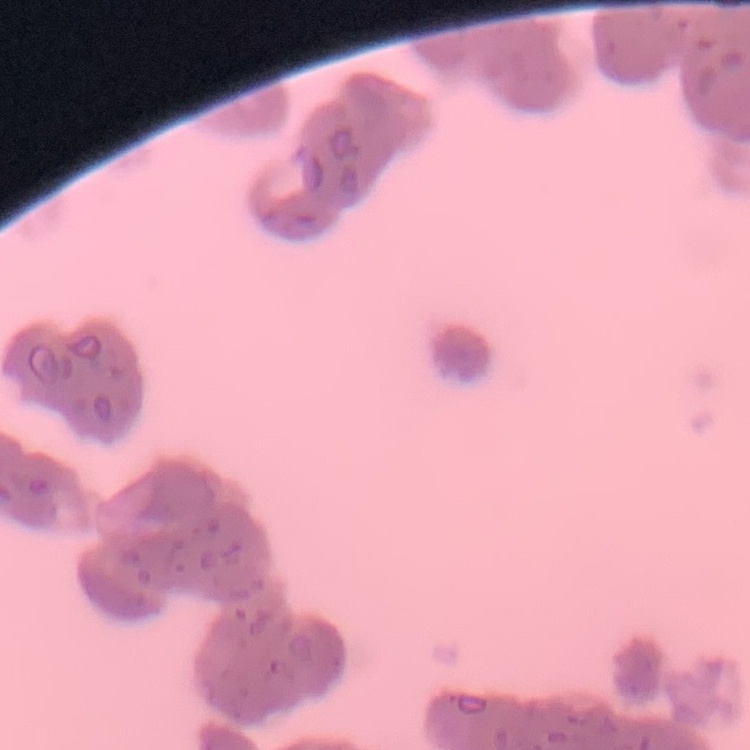

Summary:
  - Erythrocyte morphology: rouleaux formation
  - Stain: Field's or Giemsa
  - Preparation: thin peripheral smear
  - Image type: one tile cut from a larger photomicrograph